State which cell type is depicted.
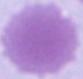
An erythrocyte.

Summary:
  - Modality: micrograph
  - Magnification: 1000x